Comment on the morphology of the red blood cells.
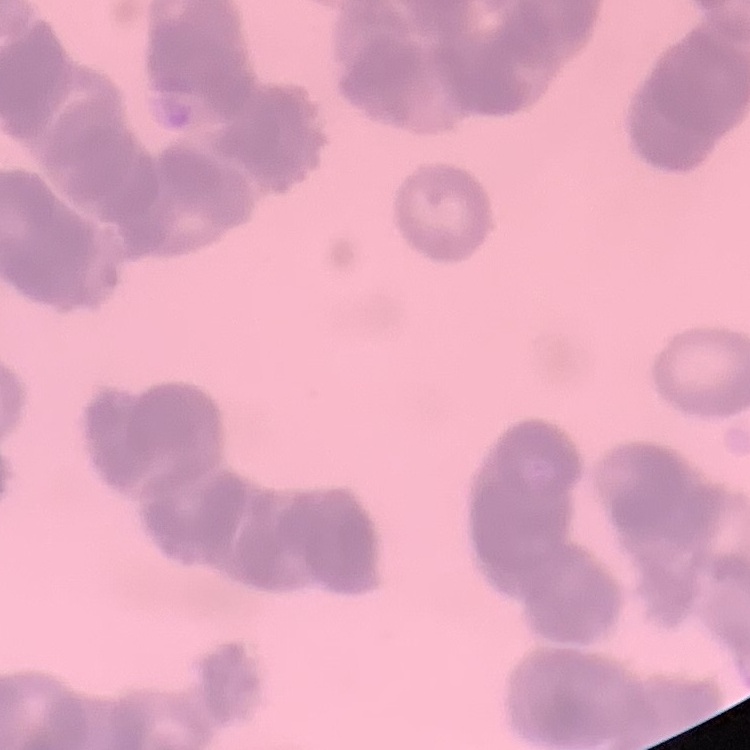

Rouleaux formation.

Stained with either Field's or Giemsa. Square crop of a larger photomicrograph. Thin blood film.